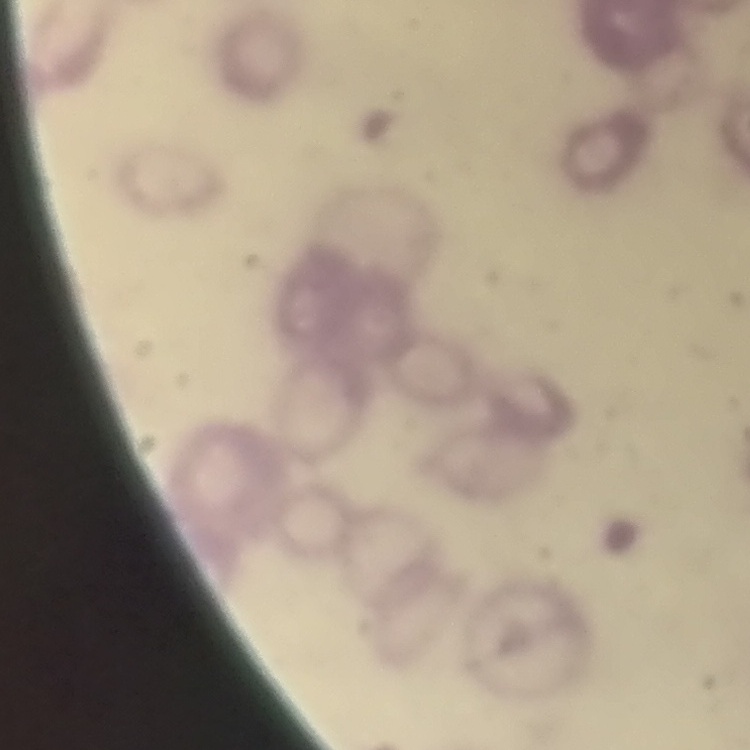
The red blood cells exhibit rouleaux formation. Thin peripheral smear. Field's or Giemsa stain. Square crop of a larger photomicrograph.